Evaluate for malaria.
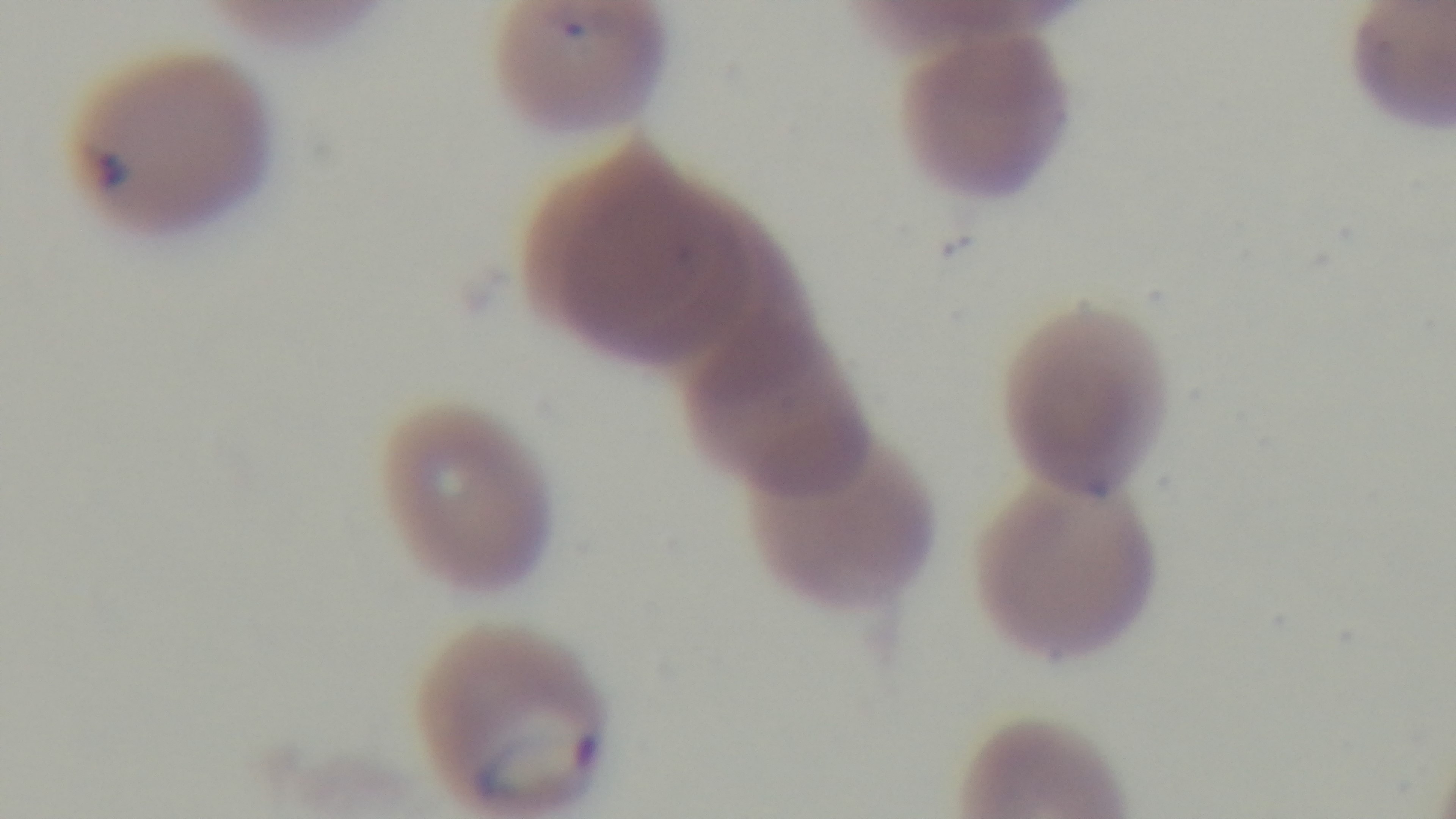

Infected.

{
  "preparation": "thin blood film",
  "field_of_view": "single",
  "modality": "light microscopy",
  "capture": "mounted 4K digital camera",
  "stain": "Giemsa",
  "objective": "100x oil immersion"
}